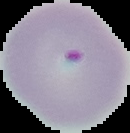
result = malaria parasites detected
image size = 130×133 pixels
preparation = thin blood smear
image type = segmented cell region with the area outside set to black